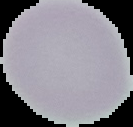

{
  "malaria_status": "uninfected",
  "preparation": "thin blood film",
  "image_size": "133×127 pixels",
  "image_type": "cell region segmented out of the field of view; surrounding area masked to black"
}